Locate every leukocyte (white blood cell).
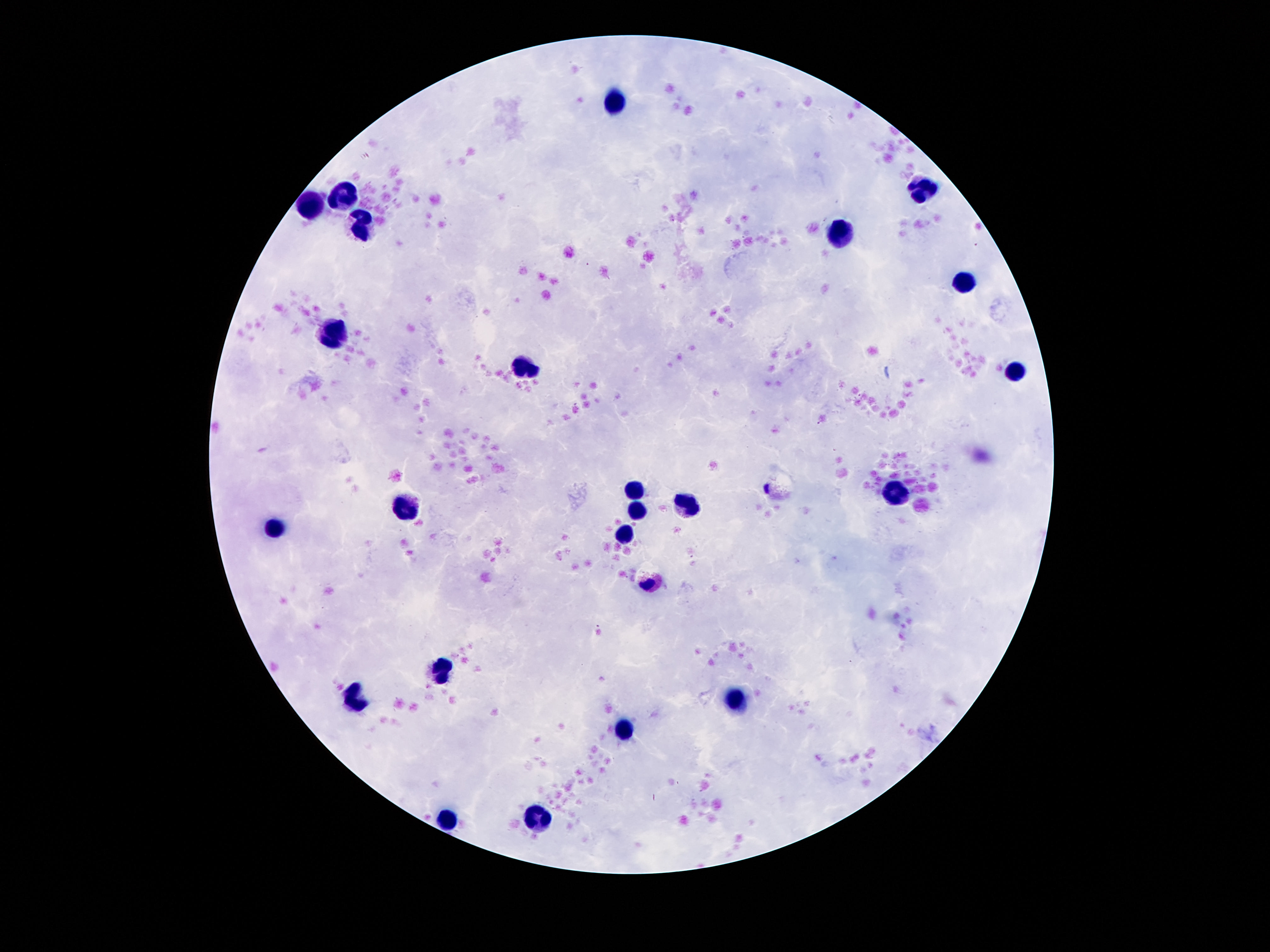
Approximate centers as {x, y} in pixels.
Leukocytes: {618, 100}, {925, 190}, {343, 198}, {314, 203}, {363, 228}, {843, 234}, {964, 278}, {335, 335}, {525, 368}, {1017, 372}, {636, 486}, {894, 491}, {689, 505}, {409, 507}, {638, 507}, {277, 528}, {624, 532}, {443, 668}, {357, 700}, {736, 700}, {622, 729}, {538, 815}, {447, 819}.

Photographed through the microscope eyepiece with a smartphone camera. Thick peripheral-blood smear. 100x magnification. One field from this slide. Giemsa-stained preparation. Image is 1270×952 pixels. Patient malaria status: not infected.